Outline every artifact (platelet-like body, stain precipitate, or debris).
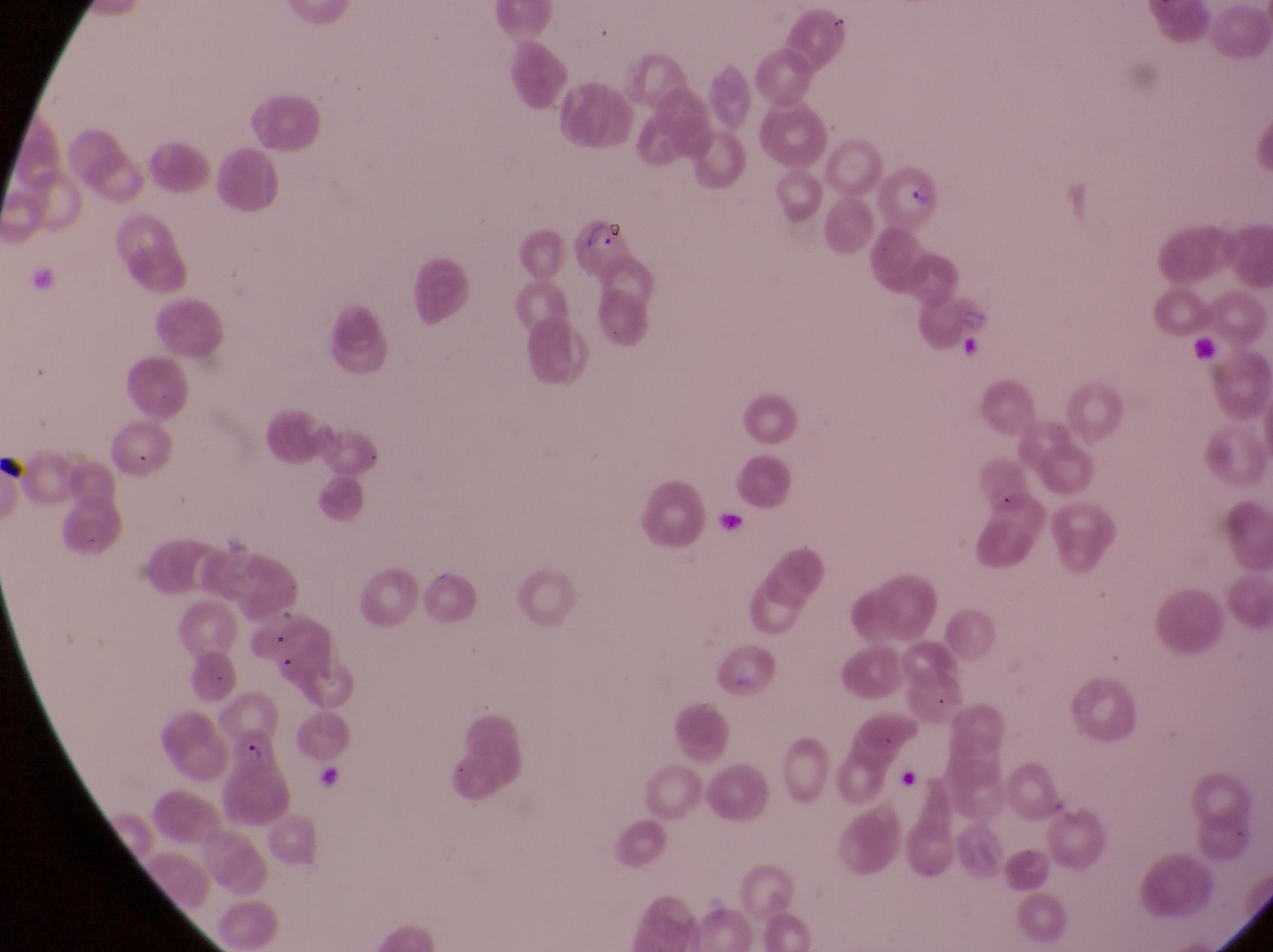
Approximate bounding boxes as left top right bottom in pixels.
Artifacts (platelet-like body, stain precipitate, or debris): 1181 334 1218 362; 889 757 916 794.

{
  "image_size": "1273×952 pixels",
  "parasitised_red_blood_cell_locations": "approximate bounding boxes as left top right bottom in pixels: 869 167 949 229; 571 227 626 266; 230 732 299 829",
  "capture": "smartphone photograph through the eyepiece of an Olympus CX-23 microscope",
  "magnification": "1000x",
  "field_of_view": "single",
  "preparation": "thin blood film",
  "country": "Uganda"
}